Give the position of every leukocyte.
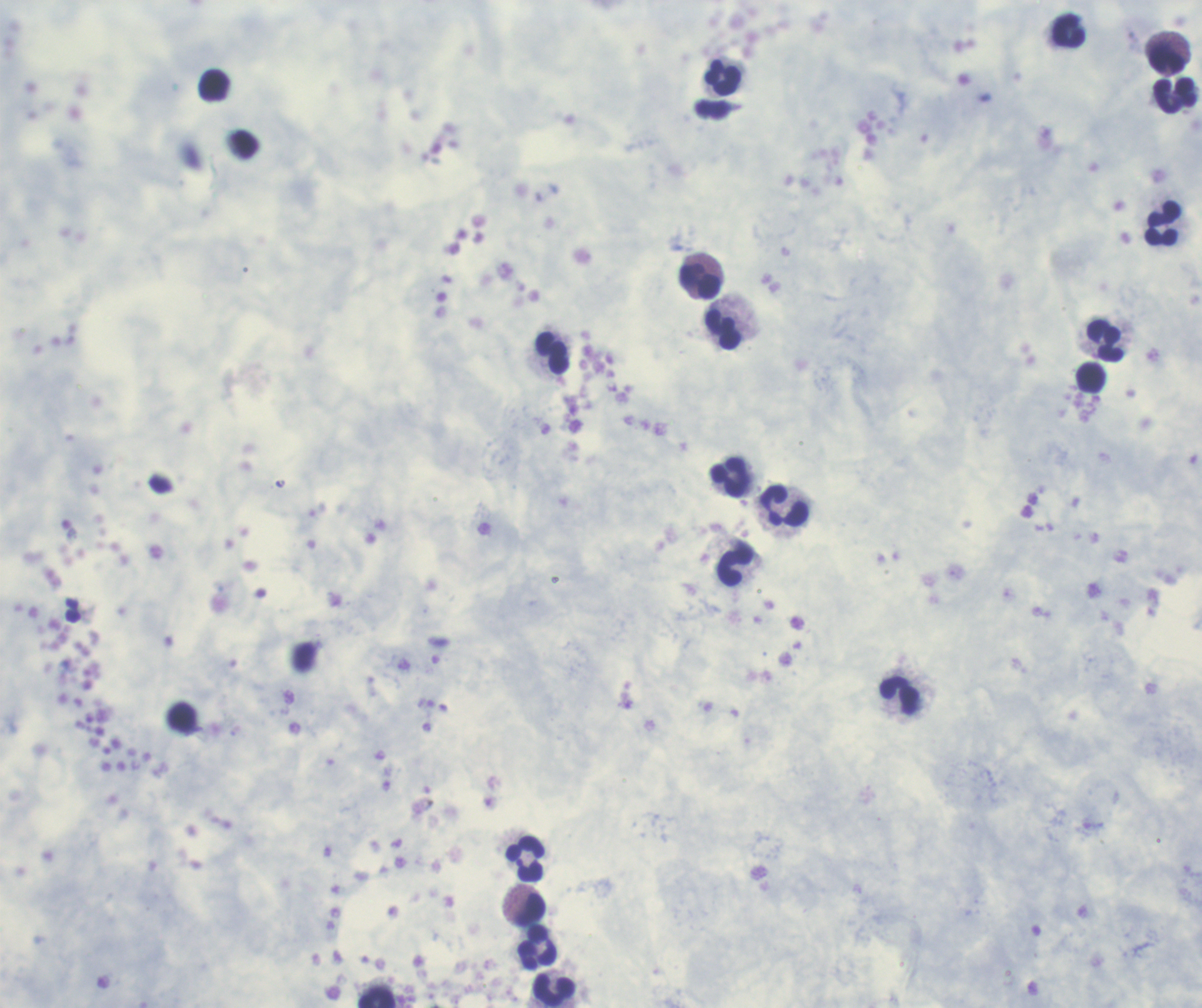

Approximate centers as (x, y) in pixels.
Leukocytes: (1068, 30), (1166, 61), (722, 77), (214, 85), (1174, 95), (1163, 223), (700, 282), (723, 329), (1106, 341), (552, 353), (1091, 377), (729, 477), (784, 506), (734, 565), (899, 695), (524, 859), (529, 910), (537, 946), (554, 989), (377, 997).

Summary:
  - Preparation: thick blood smear
  - Stain: Romanowsky
  - Magnification: 100x
  - Background quality: unsatisfactory
  - Field of view: single
  - Context: previously used in a real diagnosis
  - Result: no Plasmodium parasites seen
  - Coloration quality: good
  - Image size: 1202×1008 pixels